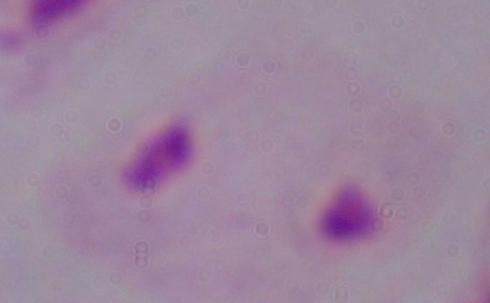

A trichomonad is seen. Photomicrograph. 1000x magnification.